Name the blood parasite species.
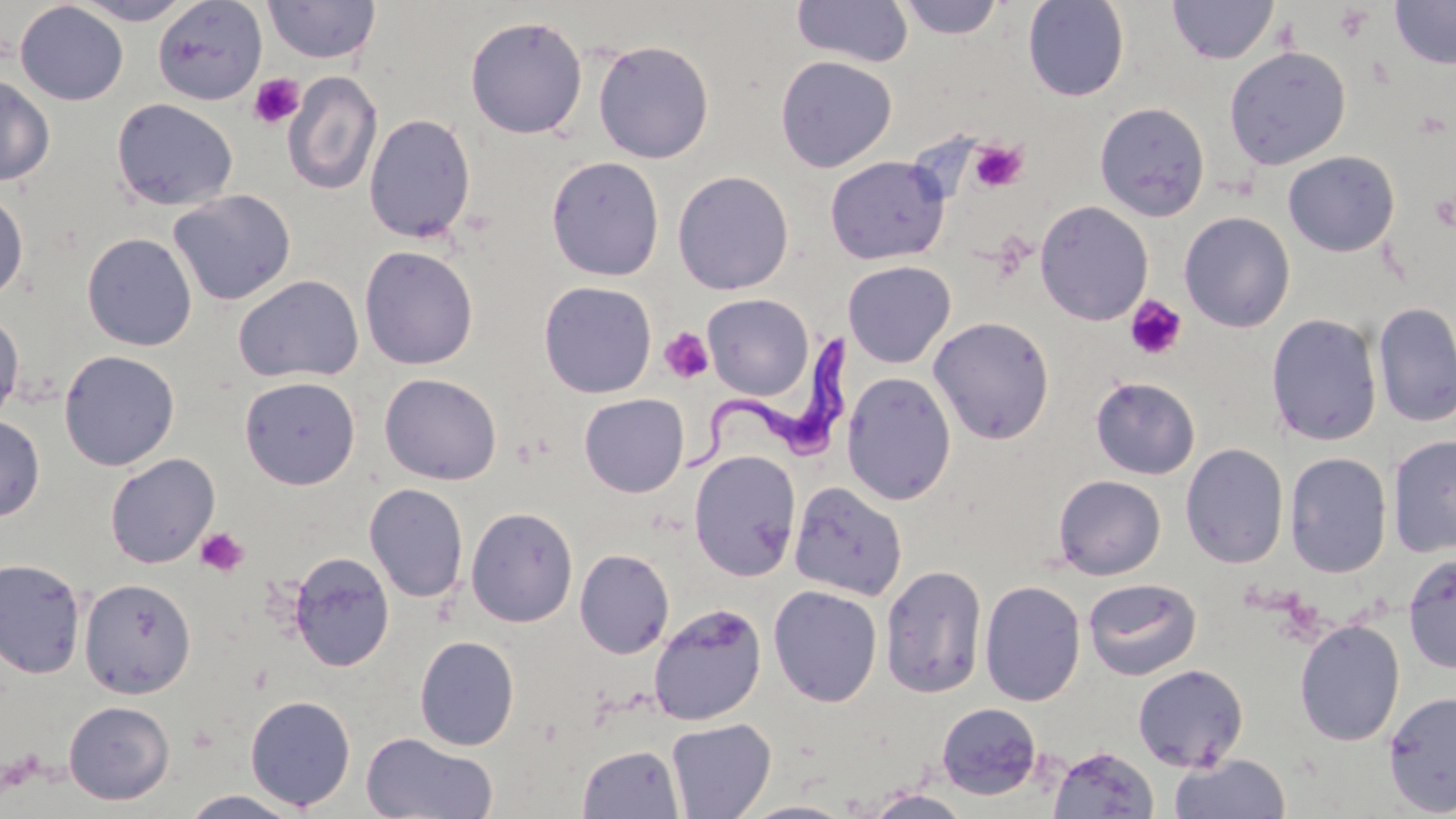
Trypanosoma brucei.

Approximate bounding boxes as [x1, y1, x2, y2] in pixels. Platelet locations: [247, 72, 306, 131], [969, 139, 1029, 193], [1125, 295, 1187, 360], [659, 327, 714, 384], [194, 528, 250, 578]. Uninfected red blood cell locations: [70, 0, 195, 25], [152, 0, 268, 105], [263, 0, 381, 64], [791, 0, 914, 68], [896, 0, 1005, 39], [1022, 0, 1130, 101], [1167, 0, 1277, 64], [1389, 0, 1456, 69], [14, 2, 128, 105], [465, 15, 588, 139], [593, 40, 715, 164], [1224, 45, 1351, 170], [775, 55, 897, 172], [283, 71, 383, 195], [0, 74, 55, 186], [111, 97, 238, 211], [1094, 101, 1210, 221], [363, 113, 477, 243], [1283, 150, 1400, 257], [546, 155, 664, 280], [825, 156, 950, 264], [672, 170, 794, 295], [0, 187, 28, 303], [168, 189, 297, 306], [1035, 200, 1154, 325], [1178, 211, 1296, 333], [81, 232, 197, 351], [359, 245, 479, 370], [842, 260, 956, 368], [232, 274, 364, 383], [538, 280, 657, 398], [702, 293, 814, 399], [1373, 300, 1456, 429], [0, 309, 25, 425], [1266, 313, 1383, 446], [929, 316, 1055, 444], [59, 350, 180, 470], [842, 371, 957, 506], [379, 373, 502, 485], [239, 376, 360, 490], [1090, 376, 1200, 479], [579, 393, 689, 497], [0, 414, 45, 522], [1386, 434, 1456, 557], [1180, 443, 1288, 569], [688, 450, 801, 582], [1285, 451, 1393, 578], [105, 453, 220, 568], [1052, 474, 1166, 580], [789, 481, 908, 600], [364, 483, 468, 603], [466, 506, 578, 628], [574, 548, 675, 659], [288, 551, 395, 672], [1402, 552, 1456, 674], [0, 557, 87, 679], [880, 563, 988, 699], [79, 578, 196, 698], [1083, 578, 1202, 681], [979, 580, 1086, 707], [768, 585, 883, 706], [648, 603, 767, 725], [1294, 618, 1405, 747], [414, 635, 520, 751], [1132, 664, 1249, 772], [1383, 689, 1456, 815], [244, 695, 356, 811], [63, 700, 175, 805], [936, 702, 1043, 799], [666, 717, 777, 818], [361, 731, 499, 819], [577, 743, 684, 818], [1048, 745, 1159, 818], [1168, 752, 1291, 818], [861, 789, 975, 818], [179, 790, 306, 818], [736, 800, 859, 818]. Trypanosoma brucei locations: [686, 326, 866, 475]. One field of a larger specimen. 1000x magnification. May-Grünwald-Giemsa-stained preparation. Thin blood smear. Optical microscopy. Image is 1456×819 pixels.